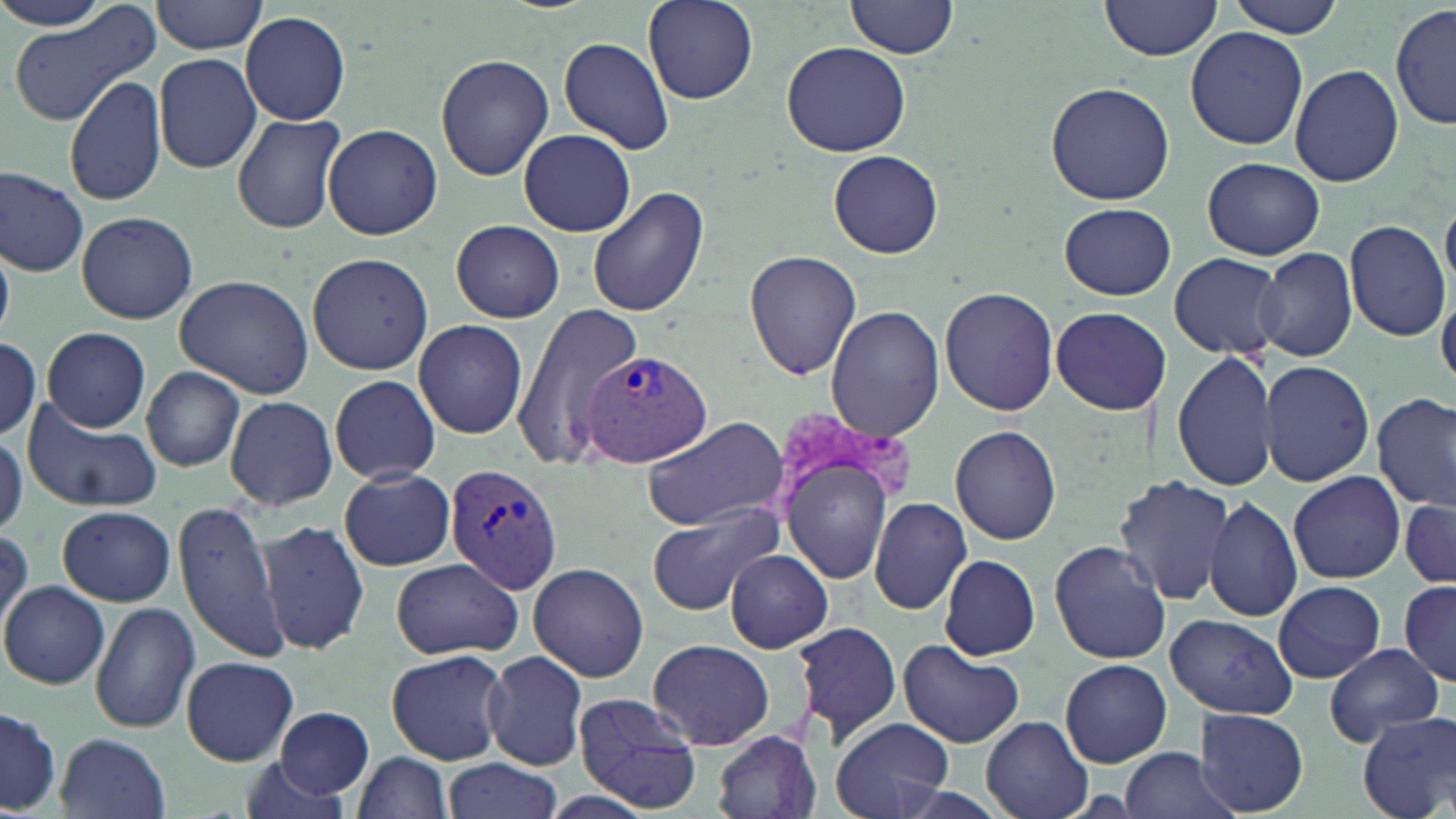

Summary:
  - Coordinate format: approximate bounding boxes as [x1, y1, x2, y2] in pixels
  - Plasmodium vivax-infected red blood cell locations: [580, 347, 712, 469], [443, 463, 563, 593]
  - Uninfected red blood cell locations: [0, 0, 119, 32], [152, 0, 267, 54], [642, 0, 757, 104], [846, 0, 959, 59], [1100, 0, 1223, 60], [1226, 0, 1347, 37], [9, 4, 161, 125], [1391, 6, 1454, 132], [241, 11, 351, 125], [1184, 26, 1309, 150], [559, 37, 675, 154], [780, 40, 914, 157], [152, 53, 261, 174], [435, 55, 554, 180], [1289, 61, 1404, 187], [65, 72, 168, 208], [1045, 81, 1174, 206], [232, 112, 348, 233], [323, 123, 445, 241], [518, 129, 633, 236], [827, 149, 943, 256], [1203, 157, 1328, 260], [0, 166, 90, 277], [587, 186, 710, 320], [1059, 202, 1176, 300], [76, 211, 198, 324], [451, 219, 565, 323], [1345, 219, 1450, 341], [0, 238, 14, 339], [745, 248, 863, 380], [1255, 248, 1358, 361], [306, 251, 434, 375], [1169, 252, 1285, 360], [174, 273, 317, 398], [938, 286, 1059, 416], [508, 303, 646, 468], [825, 306, 943, 439], [1049, 307, 1167, 415], [413, 319, 527, 438], [43, 328, 150, 432], [0, 337, 42, 441], [1171, 352, 1277, 491], [1259, 359, 1375, 486], [140, 366, 246, 470], [330, 374, 440, 485], [1373, 393, 1455, 513], [225, 396, 338, 511], [22, 401, 161, 514], [640, 415, 787, 531], [771, 420, 907, 592], [951, 424, 1062, 545], [0, 435, 25, 538], [338, 468, 456, 570], [1288, 471, 1406, 585], [1115, 474, 1237, 607], [1204, 495, 1302, 622], [1399, 495, 1456, 590], [869, 497, 972, 615], [171, 501, 293, 665], [646, 504, 785, 617], [56, 505, 176, 607], [257, 519, 371, 654], [0, 529, 31, 636], [1048, 540, 1171, 664], [725, 548, 833, 652], [938, 554, 1041, 661], [392, 558, 522, 659], [528, 562, 649, 683], [1273, 579, 1386, 683], [1, 580, 112, 689], [1399, 581, 1456, 684], [88, 604, 200, 735], [1164, 613, 1297, 717], [789, 620, 903, 746], [649, 639, 773, 750], [899, 639, 1022, 747], [1324, 644, 1443, 746], [386, 648, 511, 764], [483, 650, 588, 769], [181, 655, 299, 765], [1060, 659, 1172, 767], [572, 692, 701, 812], [0, 706, 63, 813], [274, 707, 374, 801], [1195, 709, 1309, 815], [1357, 710, 1456, 819], [980, 716, 1095, 819], [829, 717, 952, 819], [712, 730, 820, 819], [55, 733, 170, 818], [1121, 748, 1236, 819], [351, 752, 455, 819], [445, 758, 562, 818], [240, 763, 354, 818]
  - Slide-level diagnosis: Plasmodium vivax
  - Stain: May-Grünwald-Giemsa
  - Field of view: single
  - Preparation: thin blood film
  - Image size: 1456×819 pixels
  - Modality: light microscopy
  - Magnification: 1000x